Report the malaria status of this cell.
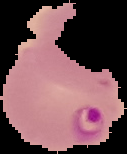
Parasitized.

preparation = thin blood smear
image size = 127×154 pixels
image type = cell region segmented out of the field of view; surrounding area masked to black